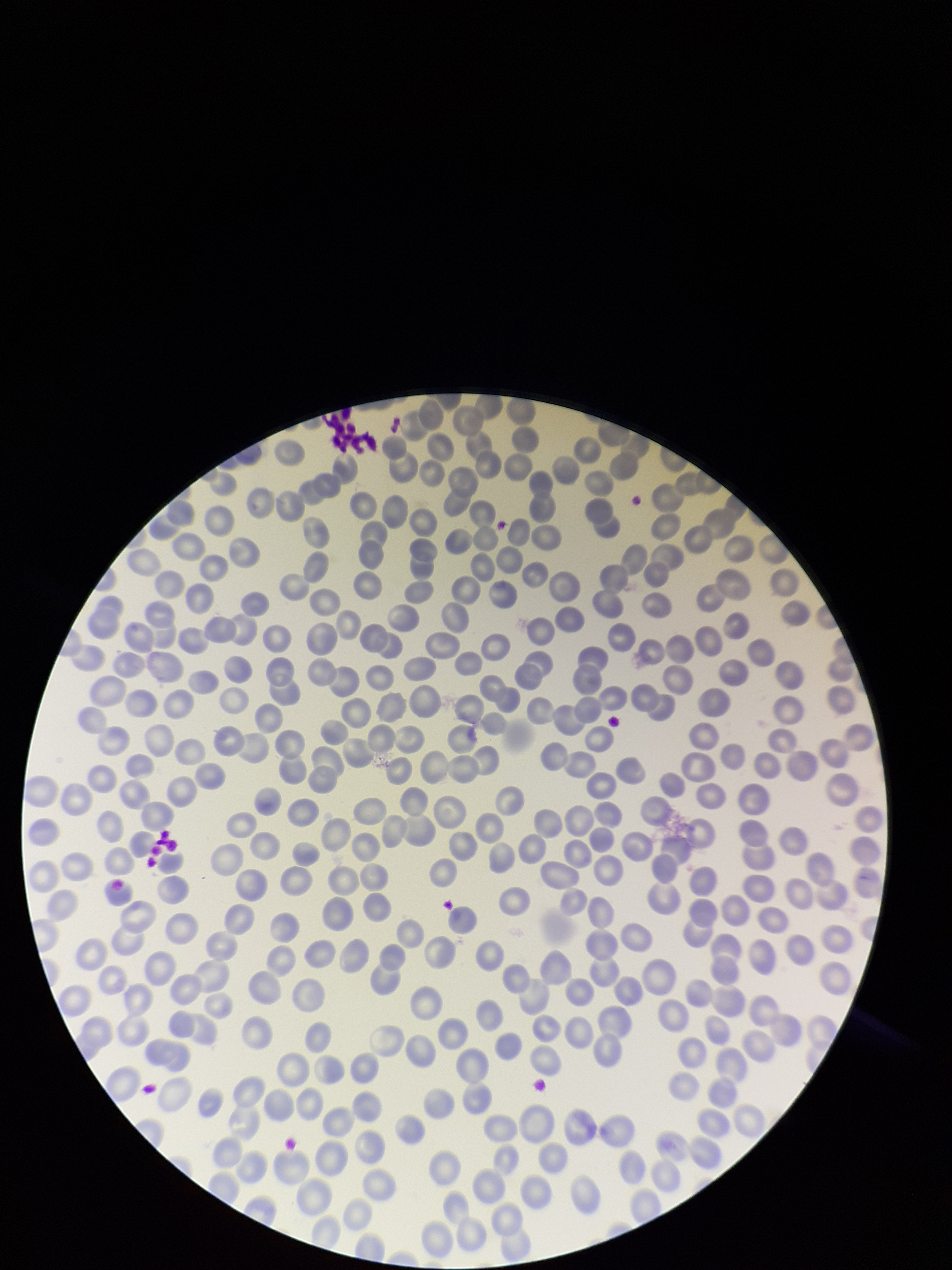

Summary:
  - Parasitized red blood cells: none seen
  - Capture: smartphone photograph through the microscope eyepiece
  - Stain: Giemsa
  - Red blood cell count: 279
  - Parasitized red blood cell count: 0
  - Patient malaria status: negative
  - Field of view: one from this slide
  - Preparation: thin
  - Image size: 952×1270 pixels